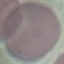
malaria_status: uninfected
stain: Giemsa
image_type: automatically extracted cell patch, resized to 64 × 64 pixels
capture: smartphone camera at the microscope eyepiece
preparation: thin blood film